Comment on the morphology of the erythrocytes.
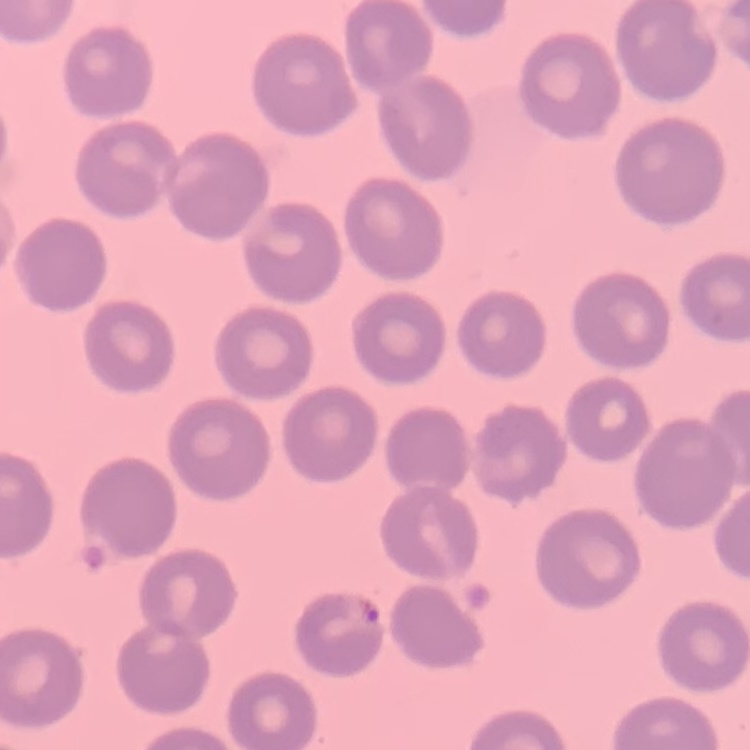
They show no rouleaux formation.

Field's or Giemsa stain. One tile cut from a larger photomicrograph. Thin blood film.